Assess this cell for malaria.
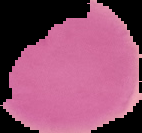
It is uninfected.

preparation = thin blood smear
image size = 142×133 pixels
image type = segmented cell region with the area outside set to black